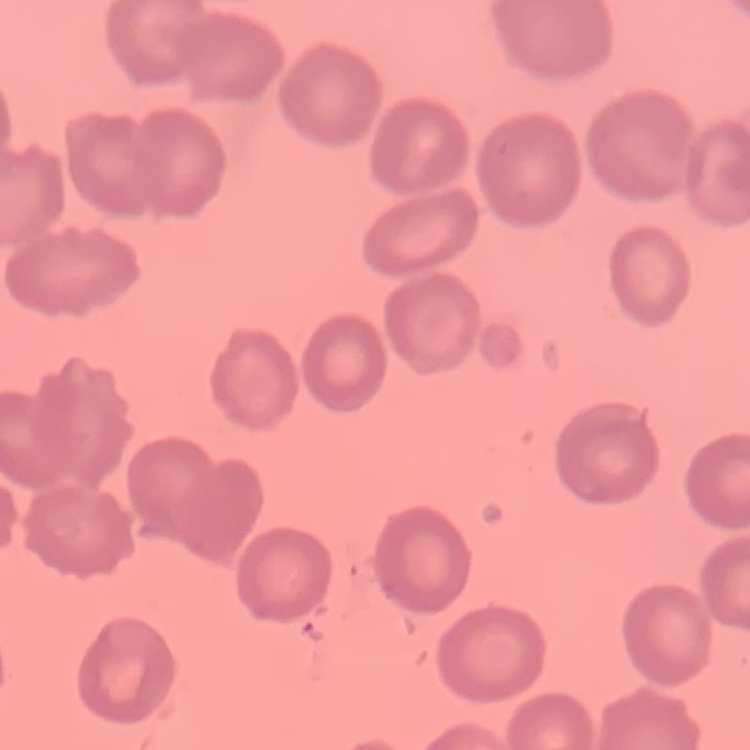

erythrocyte morphology = no rouleaux formation
preparation = thin peripheral smear
stain = Field's or Giemsa
image type = square crop of a larger photomicrograph